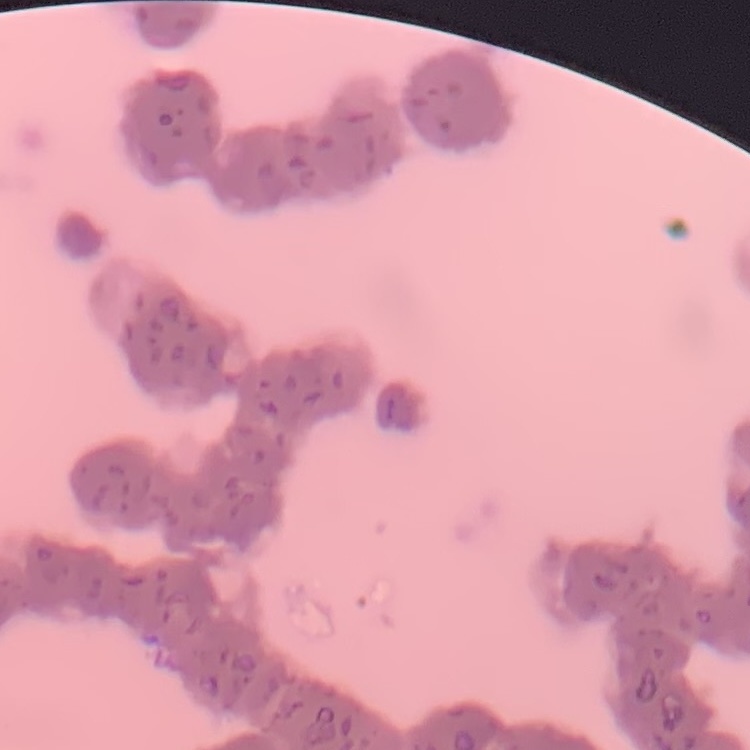

Summary:
  - Red blood cell morphology: rouleaux formation
  - Stain: Field's or Giemsa
  - Preparation: thin blood smear
  - Image type: square crop of a larger photomicrograph